Give the extent of all uninfected red blood cells.
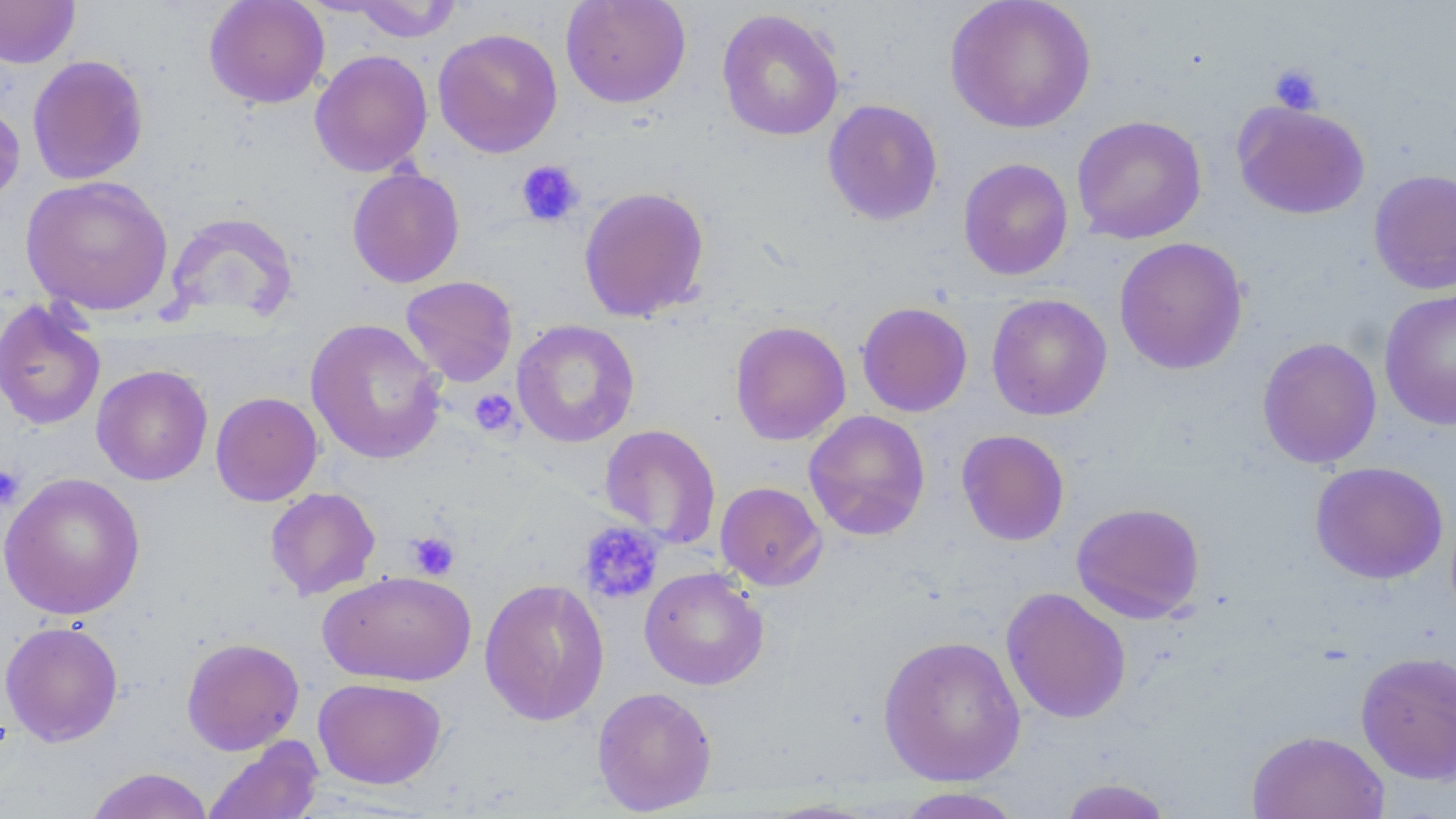
Approximate bounding boxes as named x1/y1/x2/y2 corners in pixels.
Uninfected red blood cells: (x1=0, y1=0, x2=80, y2=68), (x1=204, y1=0, x2=330, y2=109), (x1=560, y1=0, x2=692, y2=108), (x1=944, y1=0, x2=1098, y2=134), (x1=347, y1=1, x2=463, y2=42), (x1=716, y1=8, x2=845, y2=141), (x1=432, y1=27, x2=563, y2=158), (x1=309, y1=49, x2=433, y2=177), (x1=27, y1=55, x2=149, y2=185), (x1=0, y1=99, x2=25, y2=211), (x1=822, y1=99, x2=944, y2=226), (x1=1232, y1=101, x2=1370, y2=219), (x1=1071, y1=115, x2=1207, y2=244), (x1=958, y1=158, x2=1073, y2=281), (x1=347, y1=166, x2=465, y2=288), (x1=1368, y1=169, x2=1456, y2=295), (x1=21, y1=175, x2=174, y2=317), (x1=578, y1=185, x2=710, y2=323), (x1=165, y1=211, x2=297, y2=325), (x1=1113, y1=236, x2=1249, y2=375), (x1=400, y1=275, x2=518, y2=387), (x1=1379, y1=288, x2=1456, y2=431), (x1=986, y1=294, x2=1112, y2=420), (x1=0, y1=298, x2=106, y2=431), (x1=856, y1=302, x2=973, y2=417), (x1=306, y1=318, x2=448, y2=465), (x1=511, y1=319, x2=640, y2=447), (x1=730, y1=320, x2=851, y2=446), (x1=1257, y1=337, x2=1382, y2=469), (x1=92, y1=364, x2=213, y2=486), (x1=210, y1=391, x2=323, y2=506), (x1=804, y1=410, x2=931, y2=541), (x1=598, y1=424, x2=722, y2=549), (x1=956, y1=429, x2=1069, y2=546), (x1=1309, y1=461, x2=1448, y2=584), (x1=0, y1=472, x2=146, y2=620), (x1=715, y1=481, x2=827, y2=590), (x1=264, y1=487, x2=381, y2=601), (x1=1071, y1=502, x2=1205, y2=624), (x1=639, y1=566, x2=769, y2=690), (x1=318, y1=569, x2=477, y2=686), (x1=479, y1=577, x2=610, y2=726), (x1=1001, y1=587, x2=1132, y2=724), (x1=0, y1=620, x2=124, y2=746), (x1=877, y1=634, x2=1026, y2=785), (x1=181, y1=636, x2=304, y2=755), (x1=1354, y1=650, x2=1456, y2=784), (x1=313, y1=677, x2=447, y2=789), (x1=592, y1=686, x2=717, y2=815), (x1=1246, y1=729, x2=1390, y2=819), (x1=202, y1=735, x2=324, y2=819), (x1=84, y1=767, x2=215, y2=819), (x1=1056, y1=777, x2=1175, y2=819), (x1=891, y1=787, x2=1028, y2=818).

Summary:
  - Platelet locations: (x1=1268, y1=63, x2=1324, y2=115), (x1=515, y1=160, x2=585, y2=228), (x1=469, y1=388, x2=519, y2=435), (x1=0, y1=464, x2=25, y2=508), (x1=579, y1=521, x2=665, y2=605), (x1=406, y1=530, x2=460, y2=580)
  - Slide-level diagnosis: no evidence of blood parasites
  - Field of view: one of a larger specimen
  - Preparation: thin blood film
  - Magnification: 1000x
  - Modality: light microscopy
  - Stain: May-Grünwald-Giemsa
  - Image size: 1456×819 pixels